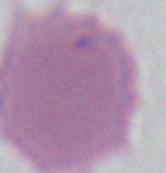

An erythrocyte is seen. Captured at 1000x magnification. Micrograph.